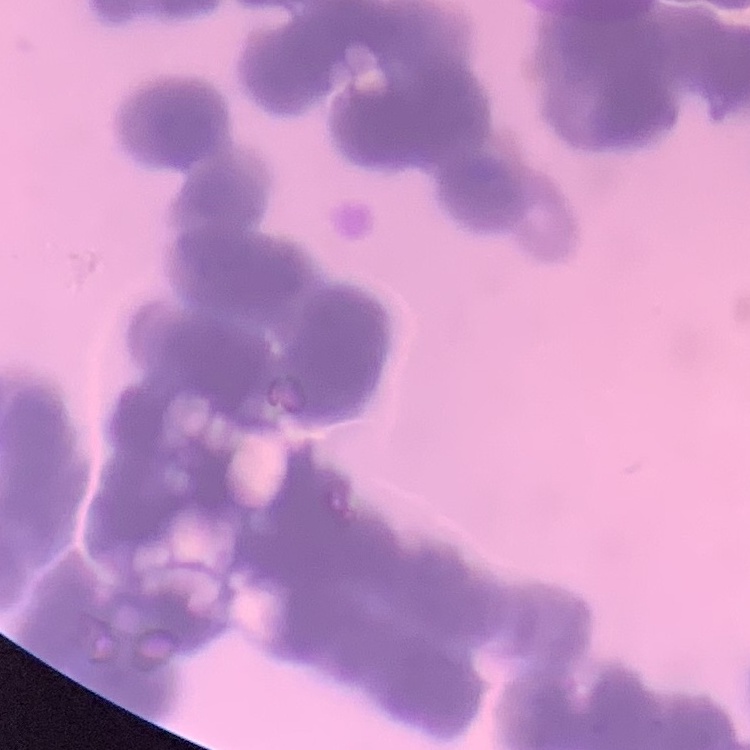

Summary:
  - Red blood cell morphology: rouleaux formation
  - Image type: one tile cut from a larger photomicrograph
  - Stain: Field's or Giemsa
  - Preparation: thin blood film